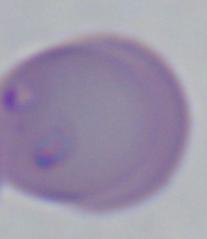

Summary:
  - Magnification: 1000x
  - Identification: Babesia
  - Modality: micrograph